State which cell type is depicted.
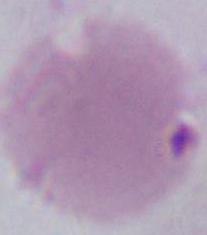
This is an erythrocyte.

modality = micrograph
magnification = 1000x